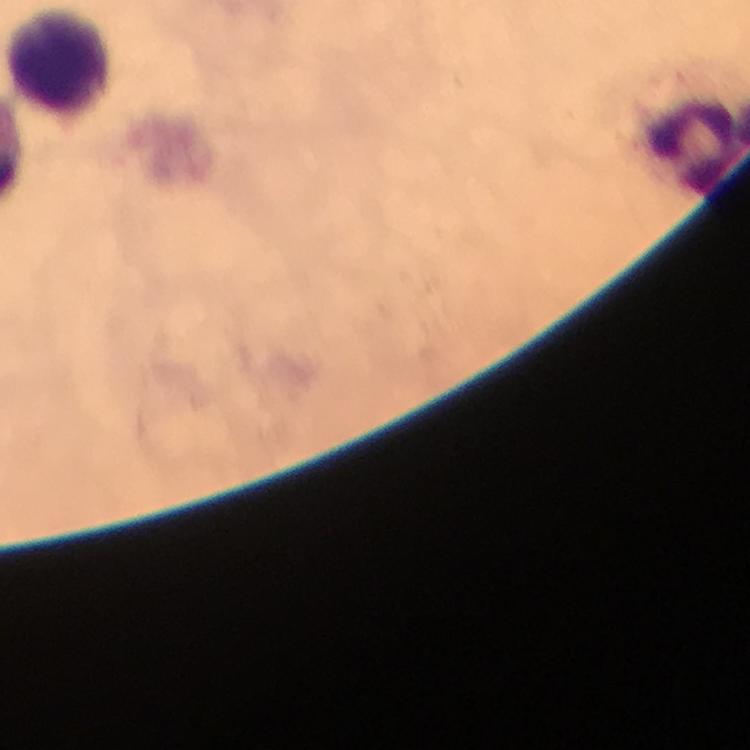
Approximate centers as {x, y} in pixels.
Summary:
  - Leukocyte locations: {59, 66}
  - Stain: Giemsa
  - Magnification: 100x
  - Cropped from: a single field of view
  - Image size: 750×750 pixels
  - Immersion oil: used
  - Capture: smartphone photograph through a microscope
  - Context: from a malaria diagnostic workup
  - Plasmodium parasites: none seen
  - Preparation: thick blood smear